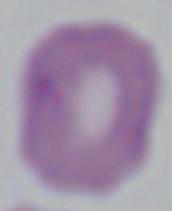

Summary:
  - Identification: Babesia
  - Magnification: 1000x
  - Modality: photomicrograph